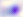
400x magnification. Toxoplasma gondii is seen. Photomicrograph.